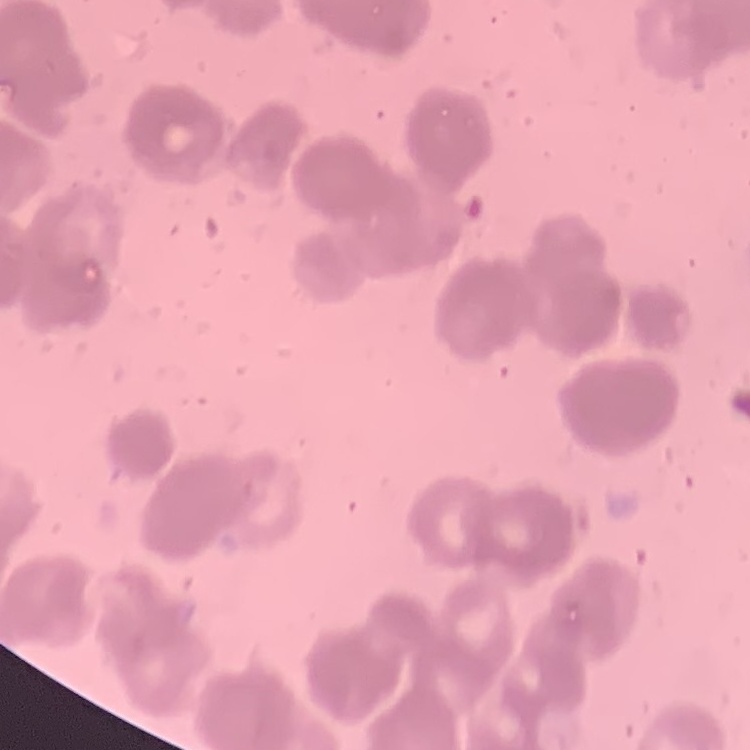
The erythrocytes exhibit rouleaux formation. Square crop of a larger photomicrograph. Stained with either Field's or Giemsa. Thin blood smear.